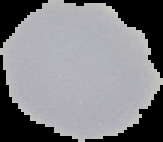

Summary:
  - Result: no malaria parasites seen
  - Image size: 163×142 pixels
  - Image type: segmented cell region with the area outside set to black
  - Preparation: thin blood film